Assess the morphology of the red blood cells.
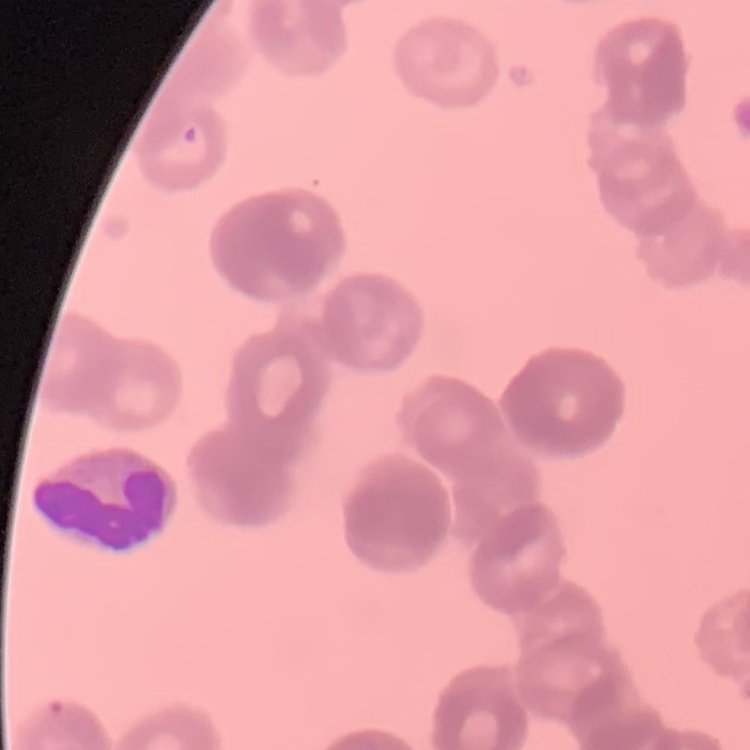
Rouleaux formation.

image type = one tile cut from a larger photomicrograph
stain = Field's or Giemsa
preparation = thin blood smear